Report the malaria status of this cell.
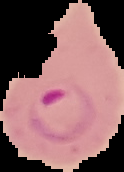
It is parasitized.

image size = 124×172 pixels
preparation = thin blood film
image type = cell region segmented out of the field of view; surrounding area masked to black